Evaluate for Plasmodium parasites.
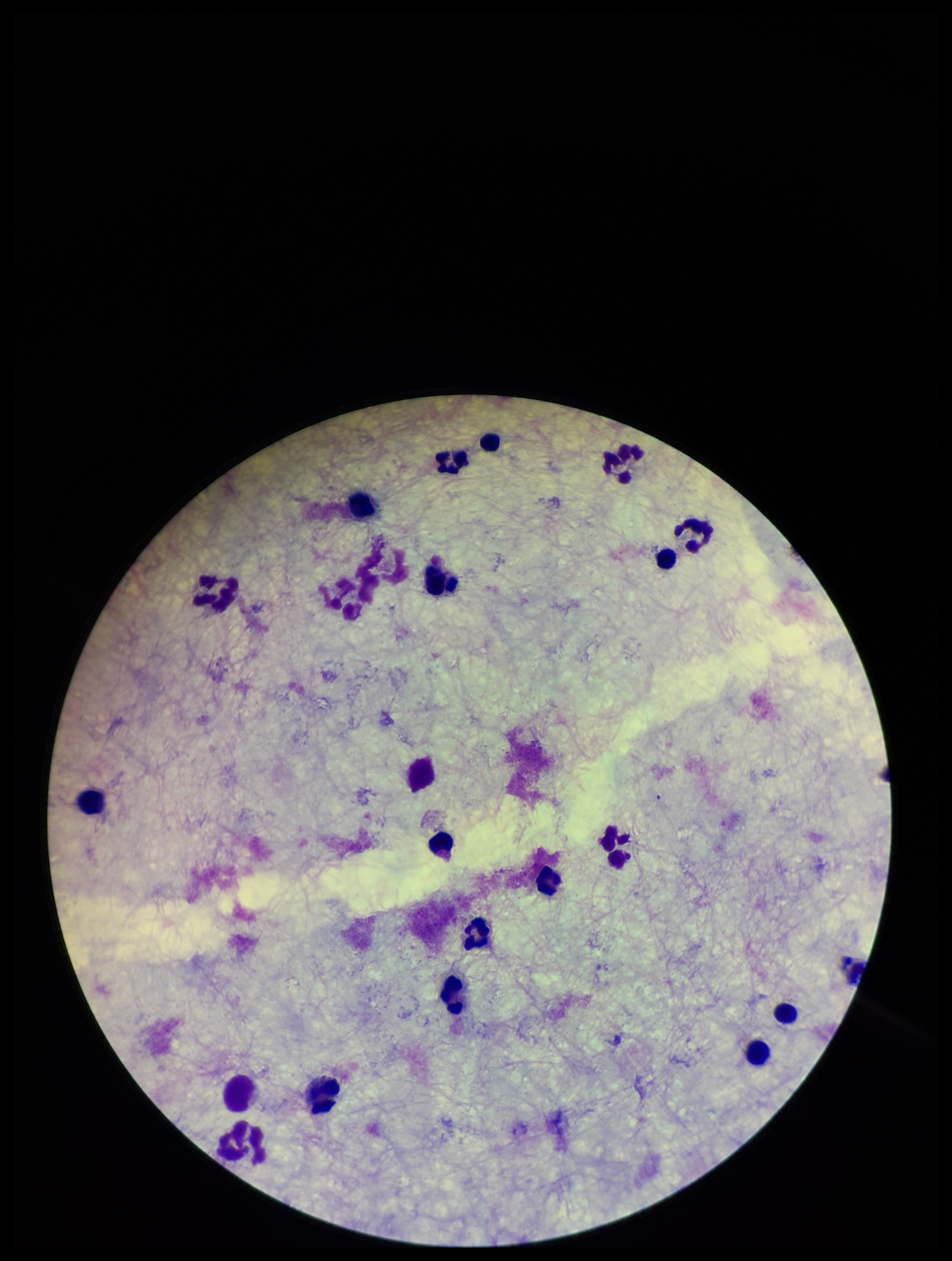
None identified.

Summary:
  - Stain: Giemsa
  - Image size: 952×1261 pixels
  - Leukocyte count: 20
  - Parasite count: 0
  - Capture: smartphone photograph through the microscope eyepiece
  - Preparation: thick blood smear
  - Patient malaria status: negative
  - Field of view: single